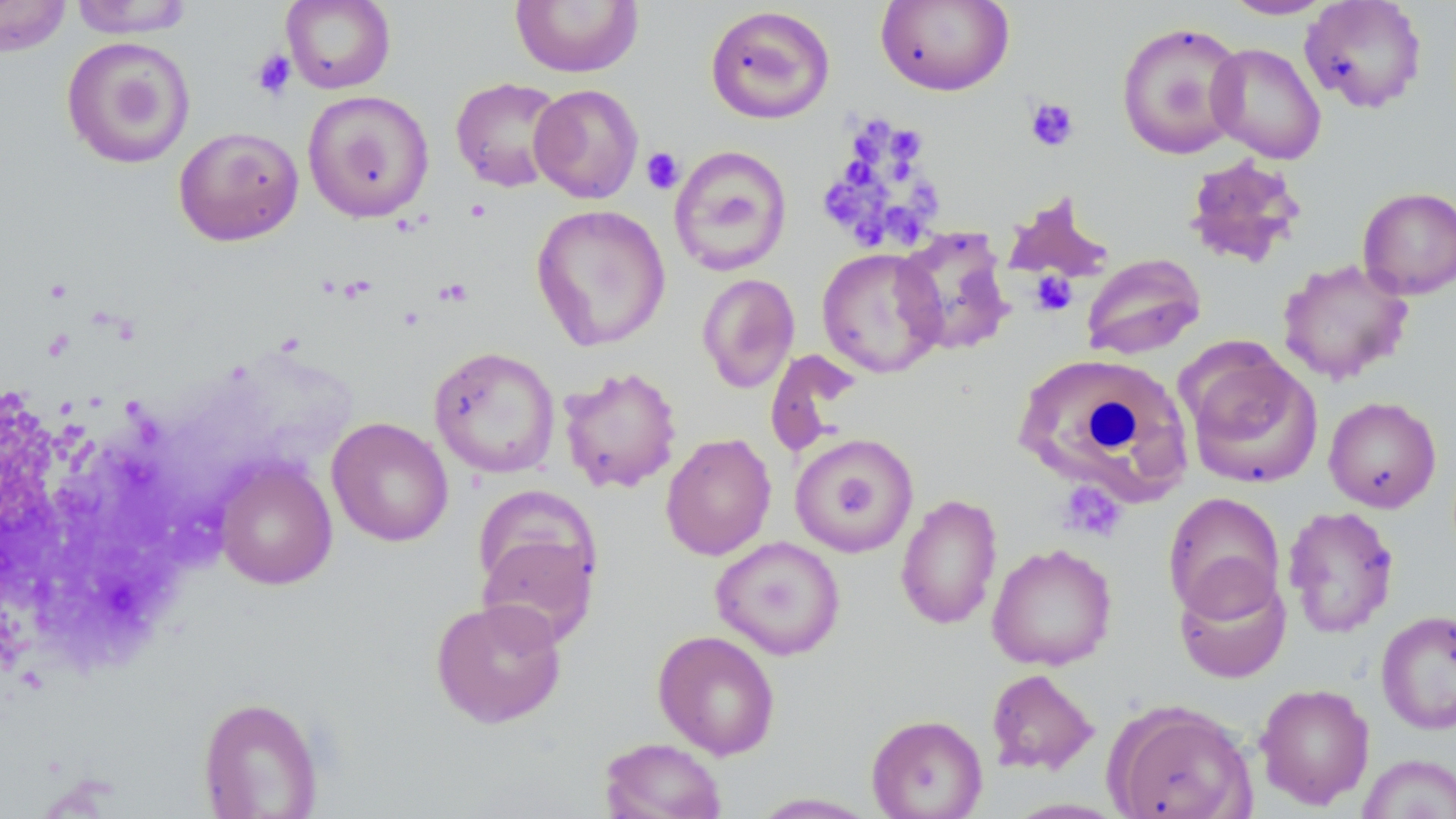

Approximate bounding boxes as named x1/y1/x2/y2 corners in pixels. Platelet locations: (x1=251, y1=49, x2=296, y2=101), (x1=1024, y1=97, x2=1079, y2=152), (x1=865, y1=115, x2=896, y2=147), (x1=890, y1=131, x2=926, y2=157), (x1=855, y1=133, x2=887, y2=164), (x1=641, y1=147, x2=685, y2=195), (x1=846, y1=160, x2=878, y2=184), (x1=898, y1=160, x2=914, y2=186), (x1=823, y1=179, x2=865, y2=219), (x1=861, y1=179, x2=897, y2=216), (x1=909, y1=182, x2=937, y2=229), (x1=883, y1=207, x2=924, y2=249), (x1=850, y1=212, x2=882, y2=245), (x1=1030, y1=271, x2=1078, y2=316), (x1=435, y1=278, x2=473, y2=307), (x1=1057, y1=481, x2=1125, y2=541). Uninfected red blood cell locations: (x1=0, y1=0, x2=73, y2=57), (x1=68, y1=0, x2=197, y2=38), (x1=281, y1=0, x2=396, y2=94), (x1=509, y1=0, x2=644, y2=78), (x1=1221, y1=0, x2=1335, y2=20), (x1=1300, y1=0, x2=1428, y2=114), (x1=876, y1=1, x2=1015, y2=96), (x1=704, y1=5, x2=836, y2=125), (x1=1115, y1=21, x2=1248, y2=159), (x1=61, y1=36, x2=196, y2=169), (x1=1206, y1=43, x2=1327, y2=163), (x1=451, y1=77, x2=567, y2=192), (x1=529, y1=84, x2=644, y2=203), (x1=303, y1=90, x2=435, y2=222), (x1=173, y1=126, x2=304, y2=246), (x1=668, y1=145, x2=793, y2=277), (x1=1182, y1=153, x2=1307, y2=269), (x1=1357, y1=187, x2=1456, y2=299), (x1=530, y1=204, x2=671, y2=352), (x1=892, y1=226, x2=1016, y2=357), (x1=817, y1=247, x2=946, y2=378), (x1=1081, y1=252, x2=1206, y2=360), (x1=1277, y1=259, x2=1414, y2=385), (x1=697, y1=273, x2=800, y2=393), (x1=428, y1=346, x2=561, y2=479), (x1=1180, y1=347, x2=1323, y2=490), (x1=765, y1=349, x2=862, y2=459), (x1=1015, y1=354, x2=1192, y2=506), (x1=558, y1=365, x2=682, y2=494), (x1=1323, y1=396, x2=1442, y2=513), (x1=326, y1=416, x2=453, y2=547), (x1=660, y1=432, x2=776, y2=561), (x1=788, y1=432, x2=921, y2=558), (x1=213, y1=458, x2=337, y2=590), (x1=1162, y1=492, x2=1286, y2=620), (x1=895, y1=493, x2=1003, y2=631), (x1=1282, y1=505, x2=1400, y2=639), (x1=475, y1=523, x2=600, y2=648), (x1=710, y1=536, x2=846, y2=661), (x1=986, y1=543, x2=1118, y2=671), (x1=1174, y1=564, x2=1291, y2=683), (x1=429, y1=597, x2=568, y2=729), (x1=1375, y1=609, x2=1455, y2=735), (x1=653, y1=630, x2=781, y2=760), (x1=985, y1=668, x2=1100, y2=776), (x1=1255, y1=682, x2=1375, y2=810), (x1=198, y1=696, x2=323, y2=818), (x1=1106, y1=702, x2=1258, y2=819), (x1=866, y1=713, x2=988, y2=818), (x1=598, y1=737, x2=727, y2=819), (x1=1357, y1=753, x2=1456, y2=819), (x1=748, y1=792, x2=881, y2=818). Slide-level diagnosis: negative for blood parasites. Image is 1456×819 pixels. May-Grünwald-Giemsa-stained preparation. Optical microscopy. Captured at 1000x magnification. Single field of view. Thin blood smear.